Assess the morphology of the red blood cells.
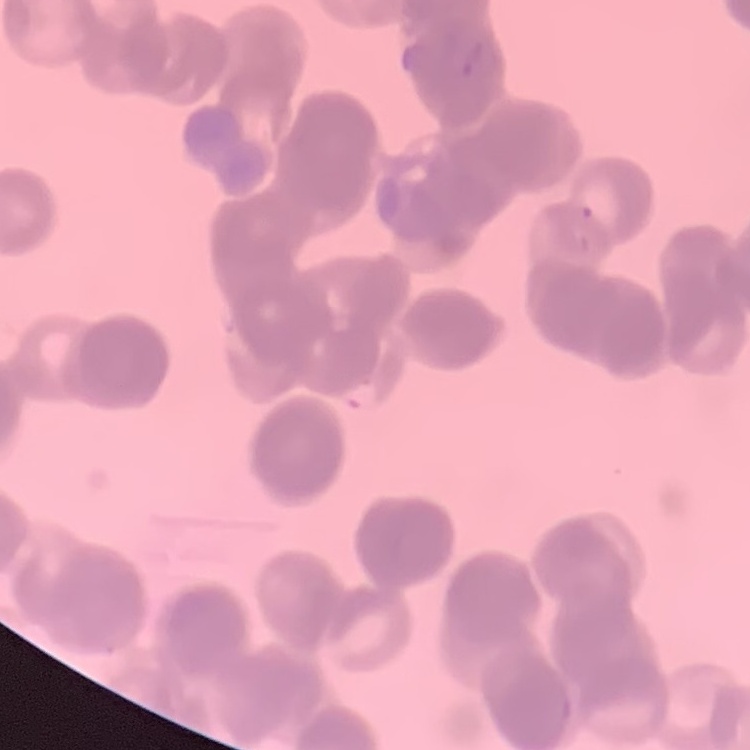
Rouleaux formation.

Stained with either Field's or Giemsa. Square crop of a larger photomicrograph. Thin peripheral smear.